Classify the preparation.
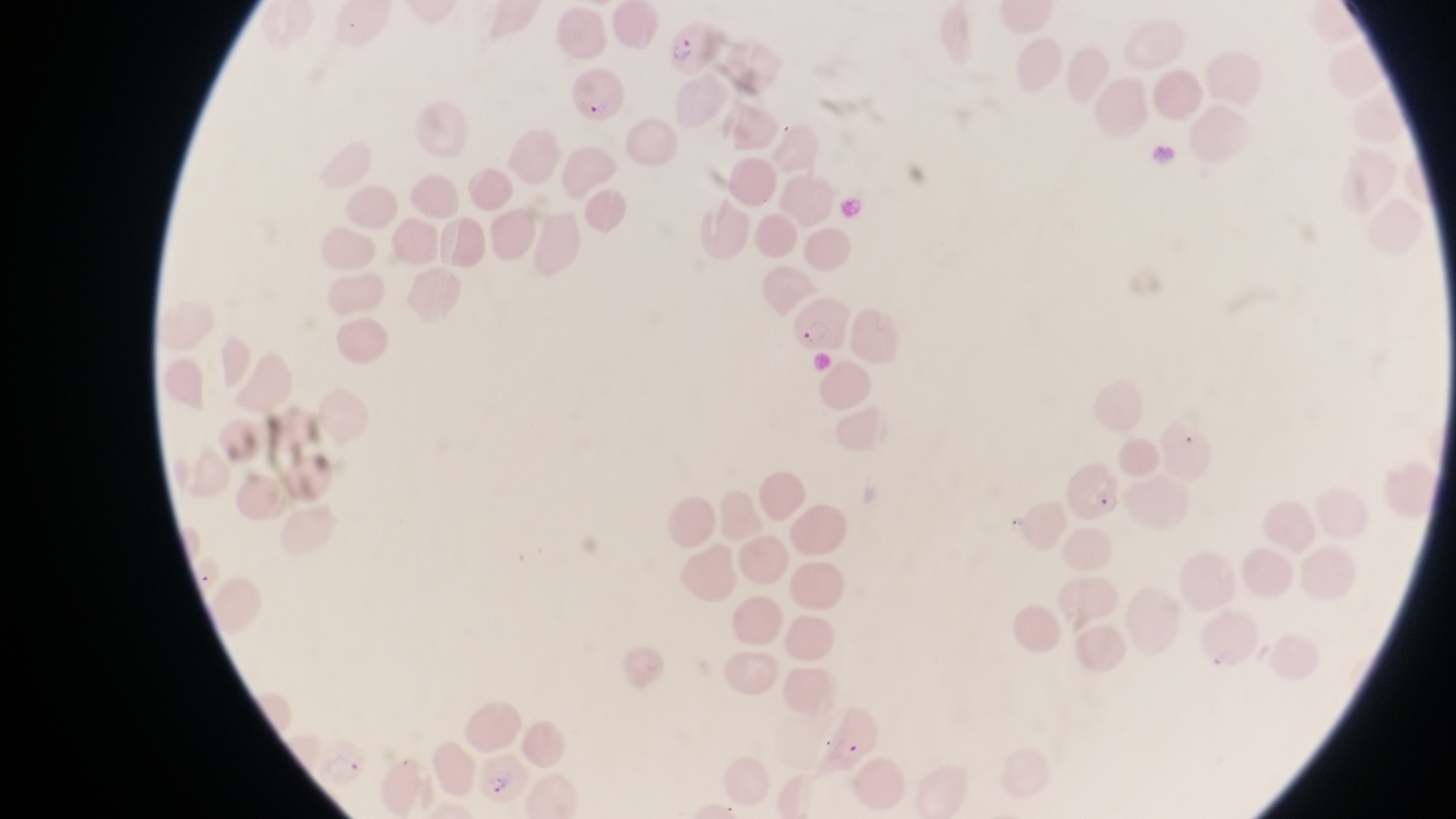

This is a thin smear.

capture = smartphone photograph through the eyepiece of an Olympus CX-23 microscope
parasitised red blood cell locations = approximate bounding boxes as left top right bottom in pixels: 670 15 718 74; 568 67 628 123; 796 297 848 364; 1067 468 1127 524; 477 750 531 802
image size = 1456×819 pixels
field of view = single
magnification = 1000x
country = Uganda